Assess the morphology of the red blood cells.
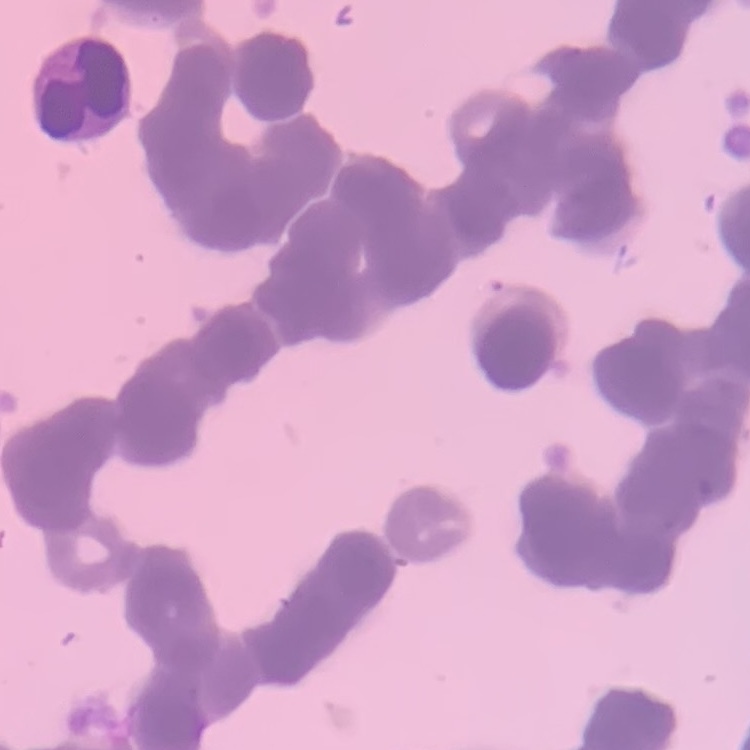

Rouleaux formation.

Square crop of a larger photomicrograph. Thin blood film. Field's or Giemsa stain.